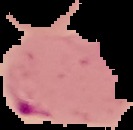

malaria_status: parasitized
preparation: thin blood smear
image_type: cell region segmented out of the field of view; surrounding area masked to black
image_size: 133×130 pixels